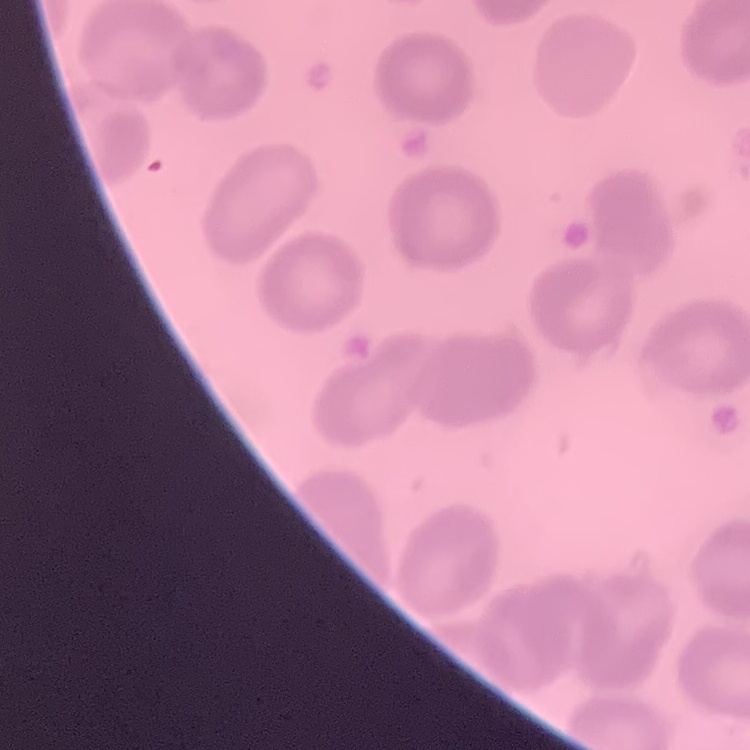
The red blood cells exhibit no rouleaux formation. Thin blood smear. One tile cut from a larger photomicrograph. Field's or Giemsa stain.